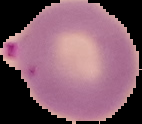
Result: Plasmodium parasites detected. From a thin blood smear. Segmented cell region on a black background. Image is 142×124 pixels.